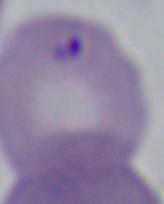

magnification = 1000x
modality = photomicrograph
identification = Babesia